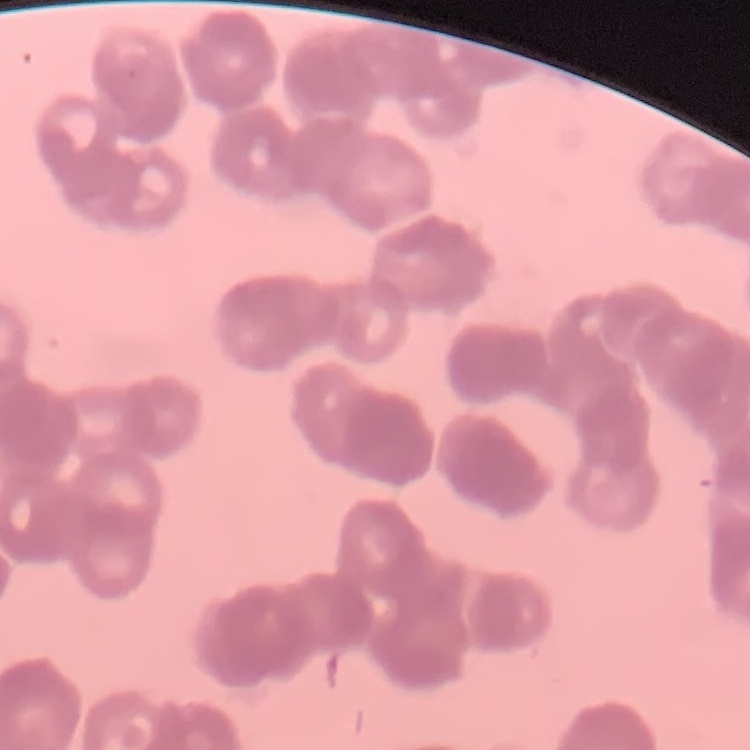
The red blood cells exhibit rouleaux formation. One tile cut from a larger photomicrograph. Thin blood film. Stained with either Field's or Giemsa.